Give the position of every Plasmodium parasite visible.
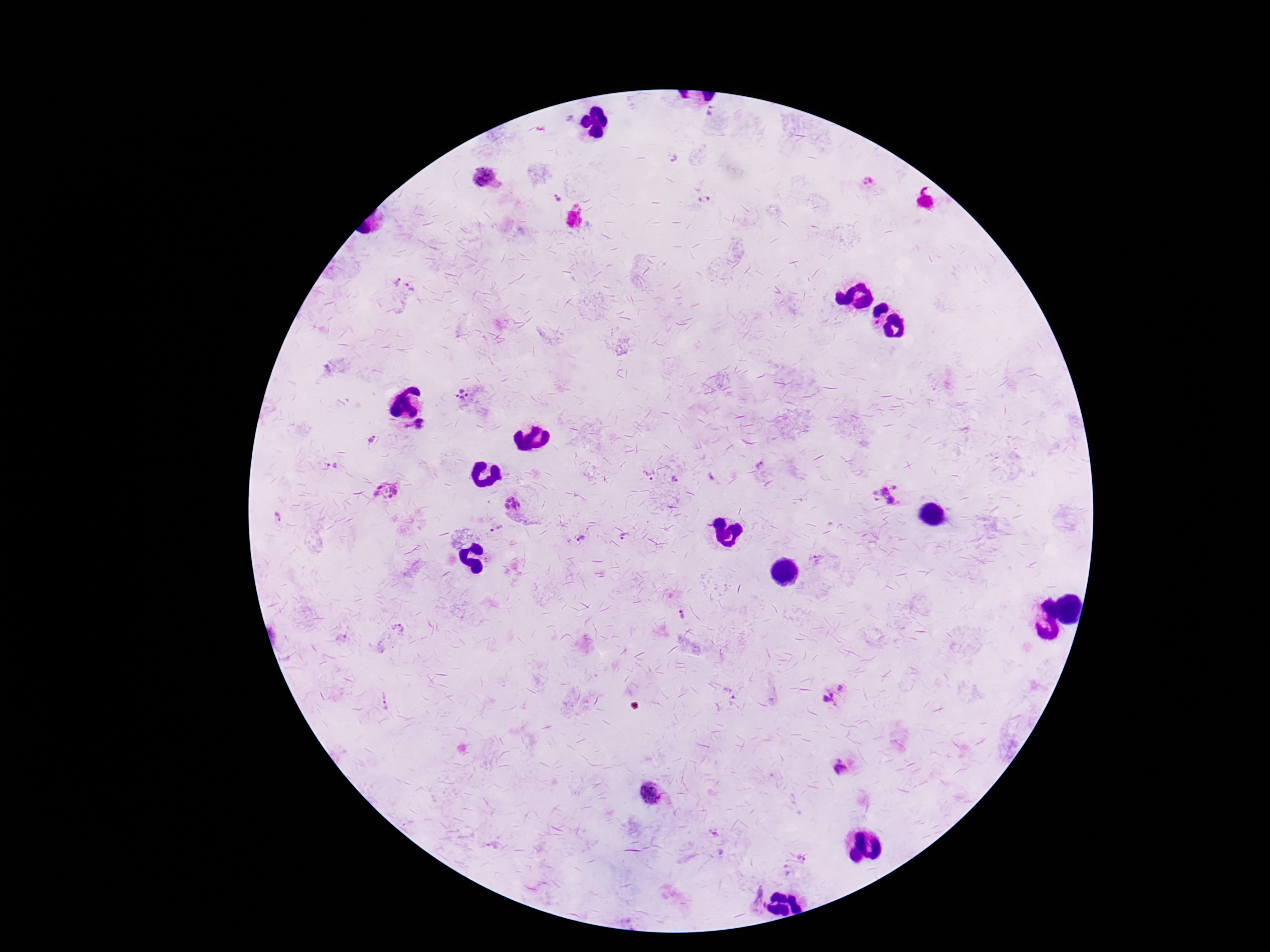

Approximate centers as (x, y) in pixels.
Plasmodium parasites: (710, 112), (568, 118), (672, 156), (489, 178), (867, 180), (558, 198), (703, 199), (398, 281), (410, 287), (877, 322), (462, 394), (420, 424), (371, 439), (331, 465), (760, 465), (650, 474), (675, 479), (380, 487), (895, 487), (394, 490), (386, 491), (884, 491), (875, 493), (377, 494), (390, 496), (876, 501), (891, 501), (512, 504), (277, 517), (492, 530), (624, 536), (582, 537), (578, 540), (818, 559), (680, 615), (399, 627), (841, 687), (386, 699), (829, 699), (840, 770), (650, 794), (801, 859), (786, 870), (758, 899).

Thick peripheral-blood smear. Smartphone photograph taken through the microscope eyepiece. 100x magnification. Image is 1270×952 pixels. Giemsa-stained preparation. Single field of view. Patient malaria status: positive.